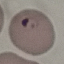
Summary:
  - Result: malaria parasites identified
  - Preparation: thin blood smear
  - Image type: cell patch, automatically extracted from a larger field of view and resized to 64 × 64 pixels
  - Capture: smartphone camera at the microscope eyepiece
  - Stain: Giemsa